Evaluate for parasitized red blood cells.
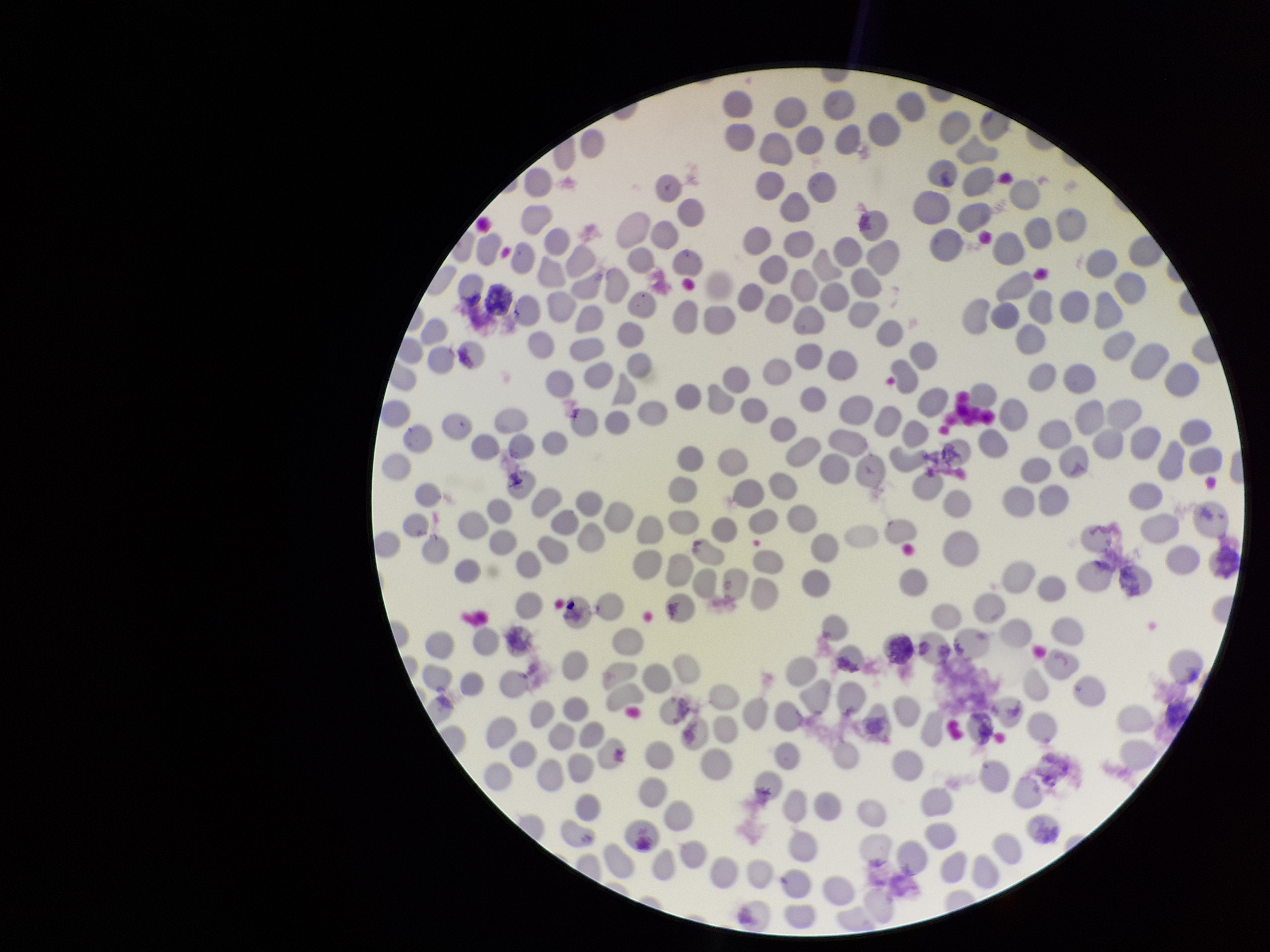

None seen.

Stained with Giemsa. Smartphone photograph taken through the eyepiece of a microscope. Red blood cell count: 254. Image is 1270×952 pixels. One field from this slide. Preparation: thin. Patient malaria status: negative. Parasitized red blood cell count: 0.